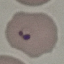

result = malaria parasites identified
preparation = thin blood smear
stain = Giemsa
image type = cell patch, automatically extracted from a larger field of view and resized to 64 × 64 pixels
capture = smartphone through the microscope eyepiece